Classify this cell by malaria status.
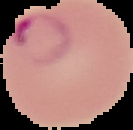
It is parasitized.

Summary:
  - Image size: 133×130 pixels
  - Preparation: thin blood film
  - Image type: cell region segmented out of the field of view; surrounding area masked to black